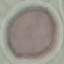
Result: negative for malaria parasites. Giemsa-stained preparation. Cell patch, automatically extracted from a larger field of view and resized to 64 × 64 pixels. Photographed with a smartphone camera at the microscope eyepiece. Thin blood film.